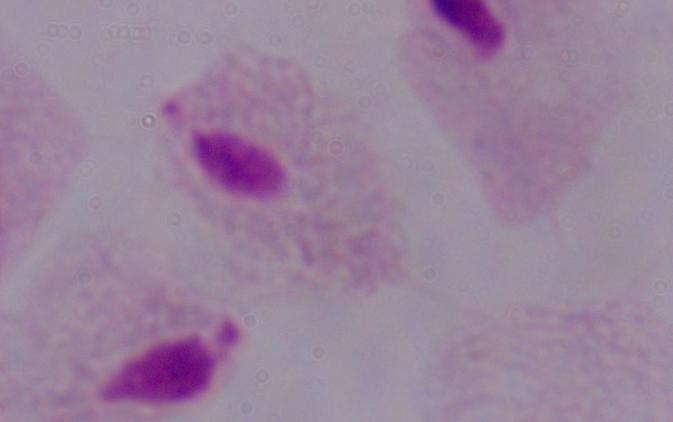

Summary:
  - Modality: photomicrograph
  - Identification: trichomonad
  - Magnification: 1000x